Assess this cell for malaria.
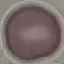
Uninfected.

Summary:
  - Image type: cell patch, automatically extracted from a larger field of view and resized to 64 × 64 pixels
  - Preparation: thin blood smear
  - Stain: Giemsa
  - Capture: smartphone camera at the microscope eyepiece